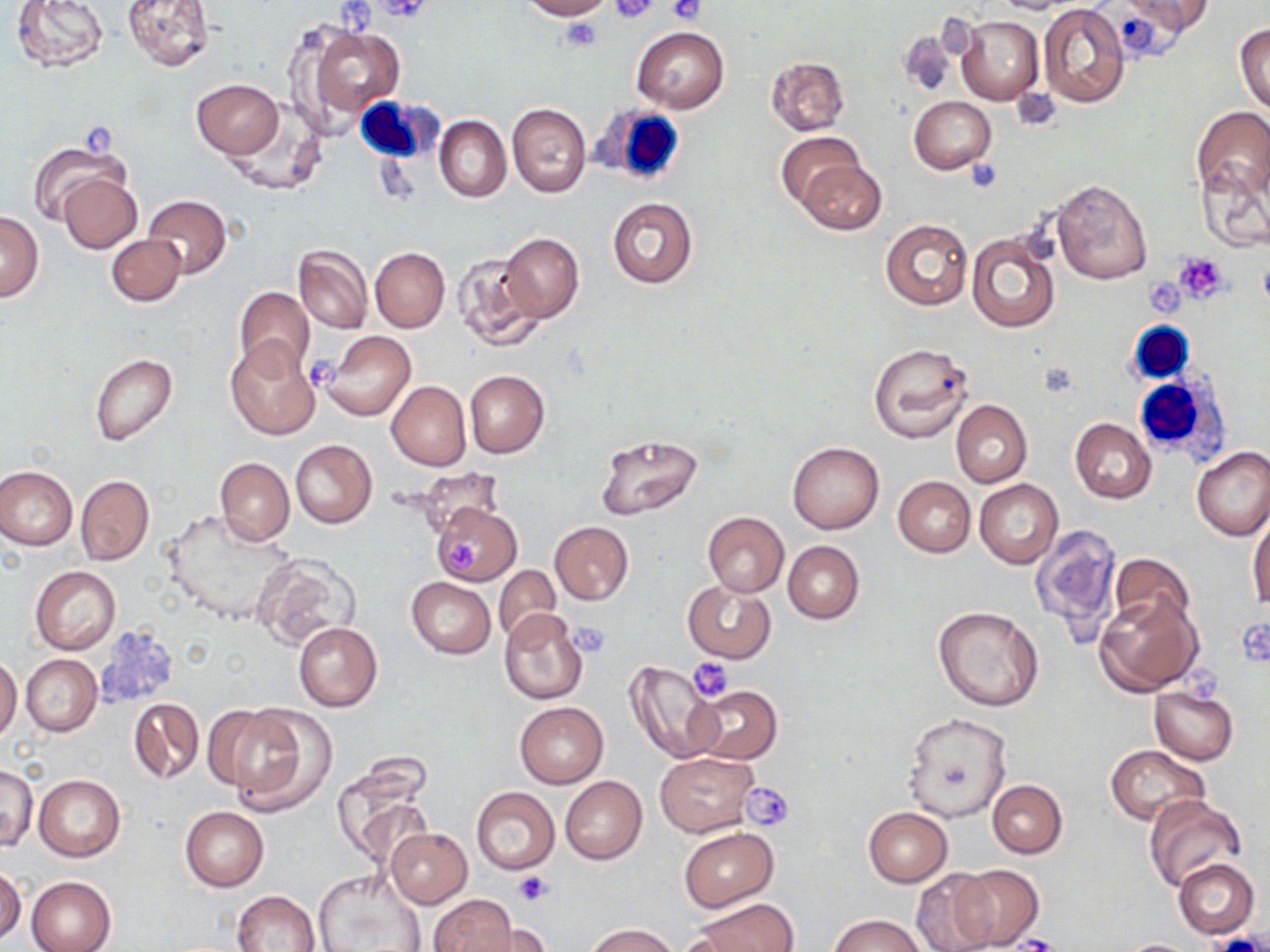

slide-level diagnosis = negative for blood parasites
field of view = single
image size = 1270×952 pixels
magnification = 1000x
preparation = thin blood film
stain = May-Grünwald-Giemsa
modality = light microscopy
uninfected red blood cell locations = approximate bounding boxes as (x1,y1)-(x2,y2) corner pairs in pixels: (10,0)-(110,73), (122,0)-(216,70), (518,0)-(613,20), (994,0)-(1081,15), (1123,0)-(1216,39), (1038,4)-(1131,109), (956,14)-(1043,106), (298,21)-(406,123), (1235,23)-(1270,115), (631,25)-(728,113), (896,31)-(957,99), (766,56)-(850,134), (191,79)-(285,158), (909,96)-(996,175), (507,103)-(591,198), (1191,106)-(1270,203), (221,112)-(327,197), (434,115)-(511,203), (776,132)-(867,212), (26,138)-(129,227), (797,159)-(885,235), (1196,162)-(1269,253), (56,173)-(142,253), (1050,179)-(1151,284), (142,194)-(232,279), (606,198)-(699,289), (0,212)-(44,301), (880,218)-(973,311), (499,233)-(584,322), (968,233)-(1060,334), (106,234)-(186,306), (293,244)-(373,334), (370,246)-(449,333), (451,252)-(543,352), (234,286)-(314,373), (320,330)-(416,422), (224,337)-(321,440), (867,341)-(974,442), (89,353)-(177,446), (464,371)-(550,457), (386,380)-(471,470), (951,400)-(1032,488), (1069,418)-(1156,503), (594,433)-(704,520), (290,439)-(378,528), (787,442)-(885,534), (1191,446)-(1270,541), (214,457)-(294,546), (0,465)-(77,549), (76,475)-(154,565), (893,476)-(974,557), (974,479)-(1063,568), (431,501)-(521,585), (162,509)-(300,626), (702,512)-(789,596), (1248,514)-(1270,610), (550,521)-(634,605), (1030,524)-(1123,640), (783,540)-(864,624), (252,553)-(362,650), (1109,553)-(1195,638), (30,565)-(121,654), (493,565)-(561,641), (406,577)-(495,659), (683,579)-(776,663), (1094,593)-(1202,696), (933,605)-(1045,712), (498,607)-(589,704), (293,621)-(382,711), (21,654)-(101,736), (0,656)-(22,742), (624,659)-(724,765), (690,685)-(781,765), (1149,686)-(1240,764), (127,697)-(204,785), (513,701)-(607,788), (223,704)-(337,815), (202,705)-(294,793), (901,712)-(1011,822), (1106,745)-(1208,825), (655,752)-(758,836), (1,764)-(37,850), (333,764)-(432,865), (34,775)-(126,861), (560,776)-(648,865), (988,780)-(1067,857), (471,786)-(560,874), (1145,795)-(1248,891), (181,807)-(268,890), (863,807)-(952,886), (386,827)-(473,908), (679,828)-(778,911), (1175,859)-(1259,939), (953,864)-(1043,949), (0,867)-(25,943), (314,867)-(428,952), (911,869)-(998,952), (26,875)-(116,952), (234,890)-(321,951), (429,895)-(519,952), (693,898)-(796,952), (830,914)-(928,952), (468,919)-(552,950), (586,924)-(678,951), (1117,938)-(1202,951)
white blood cell locations = approximate bounding boxes as (x1,y1)-(x2,y2) corner pairs in pixels: (358,95)-(439,163), (592,102)-(690,189), (1126,321)-(1193,384), (1132,373)-(1231,460)
platelet locations = approximate bounding boxes as (x1,y1)-(x2,y2) corner pairs in pixels: (610,0)-(657,24), (667,0)-(706,25), (337,1)-(378,33), (378,1)-(431,23), (559,17)-(603,53), (81,120)-(120,158), (963,161)-(1004,193), (1174,253)-(1230,302), (1150,278)-(1186,322), (303,353)-(340,394), (444,540)-(484,574), (1240,619)-(1270,670), (568,622)-(611,656), (688,658)-(734,702), (1182,666)-(1219,706), (742,781)-(795,831), (514,871)-(552,906), (1205,933)-(1264,952), (1011,935)-(1062,952)